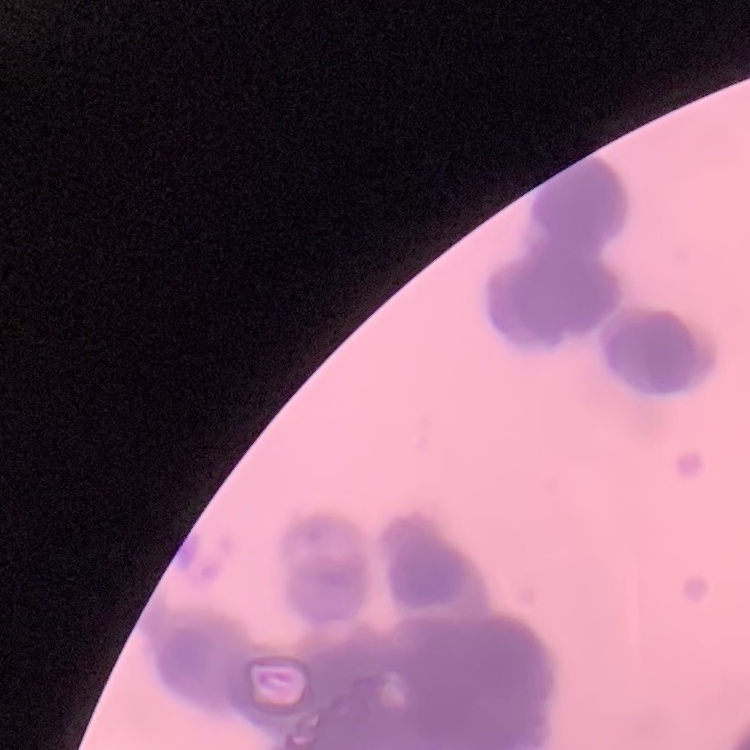
erythrocyte morphology = rouleaux formation
image type = square crop of a larger photomicrograph
preparation = thin blood smear
stain = Field's or Giemsa